Locate every Plasmodium parasite.
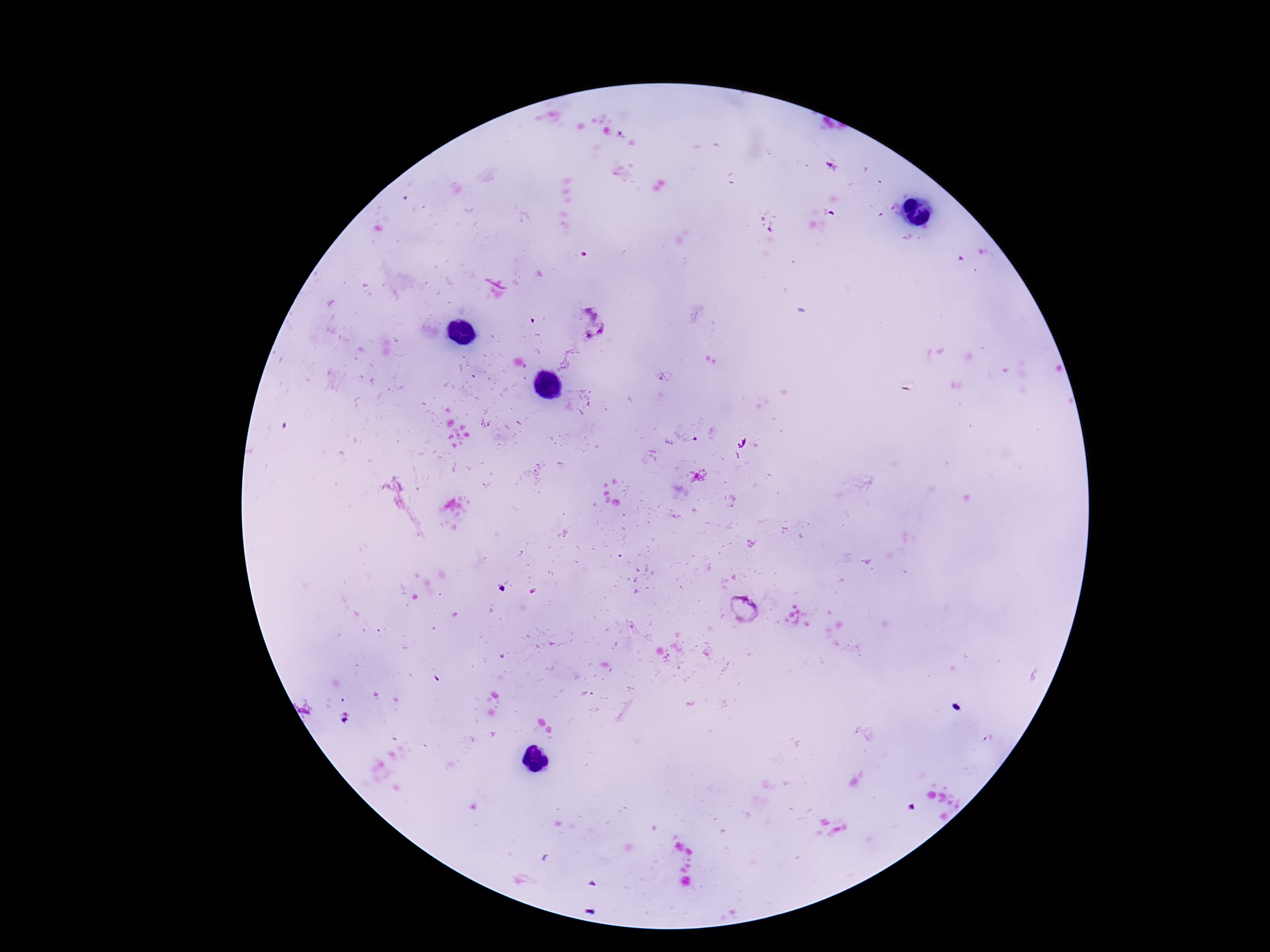
Approximate object centers, in pixels from the top-left corner.
Plasmodium parasites: (x=587, y=323), (x=743, y=608).

Summary:
  - Magnification: 100x
  - Stain: Giemsa
  - Image size: 1270×952 pixels
  - Preparation: thick blood film
  - Patient malaria status: infected
  - Capture: smartphone camera through the microscope eyepiece
  - Field of view: one from this slide